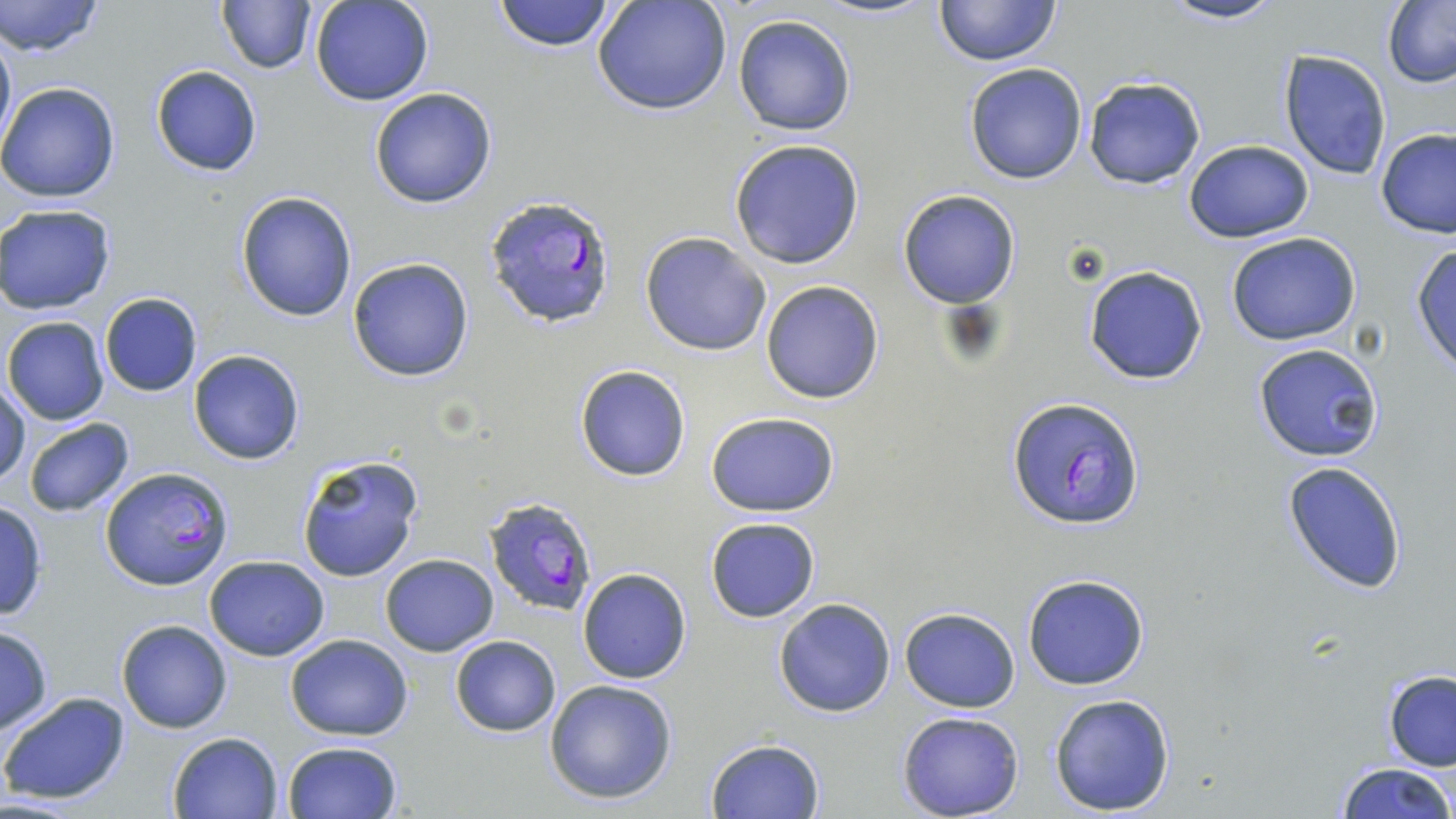

Approximate bounding boxes as (x1, y1, x2, y2) in pixels. Uninfected red blood cell locations: (0, 0, 107, 58), (216, 0, 316, 73), (311, 0, 435, 106), (492, 0, 616, 52), (592, 0, 732, 117), (933, 0, 1062, 66), (1157, 0, 1292, 25), (1381, 2, 1456, 87), (731, 14, 856, 136), (0, 22, 15, 159), (1278, 50, 1392, 180), (964, 62, 1090, 184), (150, 64, 263, 176), (1081, 75, 1208, 189), (1, 82, 121, 204), (368, 88, 497, 208), (1376, 128, 1456, 238), (729, 138, 866, 270), (1183, 139, 1313, 242), (897, 189, 1021, 309), (235, 190, 358, 321), (0, 205, 117, 314), (640, 232, 770, 356), (1227, 233, 1361, 346), (1411, 243, 1456, 373), (347, 256, 474, 383), (1084, 266, 1209, 385), (760, 281, 885, 404), (98, 292, 202, 397), (3, 317, 110, 426), (1252, 342, 1384, 462), (188, 349, 305, 465), (574, 364, 691, 482), (1, 379, 29, 487), (703, 412, 842, 516), (22, 417, 135, 516), (297, 454, 424, 582), (1281, 459, 1409, 595), (0, 502, 48, 620), (704, 516, 822, 623), (379, 554, 499, 656), (204, 555, 330, 660), (577, 568, 692, 683), (1022, 572, 1150, 691), (772, 599, 896, 718), (900, 607, 1019, 712), (116, 619, 233, 734), (0, 626, 54, 734), (284, 633, 413, 740), (449, 635, 561, 737), (1384, 672, 1456, 771), (543, 679, 678, 804), (1, 690, 131, 806), (1048, 692, 1177, 816), (897, 712, 1023, 819), (168, 731, 285, 819), (704, 737, 825, 819), (281, 741, 402, 819), (1332, 760, 1456, 819). Plasmodium falciparum-infected red blood cell locations: (484, 192, 620, 328), (1008, 397, 1143, 530), (101, 467, 230, 590), (482, 495, 599, 616). Slide-level diagnosis: Plasmodium falciparum. Image is 1456×819 pixels. Optical microscopy. Single field of view. Captured at 1000x magnification. Thin blood smear. May-Grünwald-Giemsa-stained preparation.